Give the extent of all Plasmodium malariae-infected red blood cells.
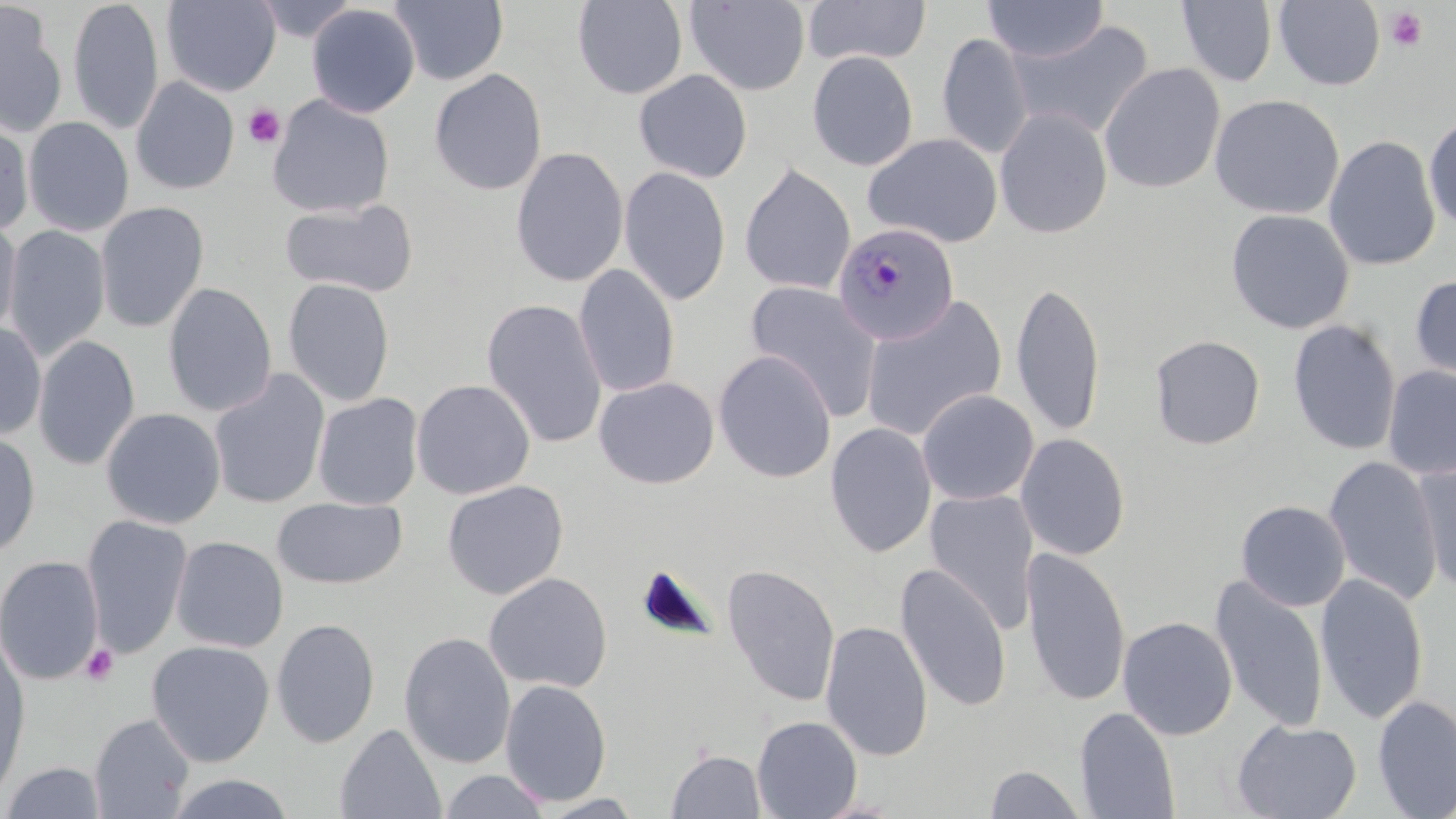
Approximate bounding boxes as named x1/y1/x2/y2 corners in pixels.
Plasmodium malariae-infected red blood cells: (x1=832, y1=222, x2=959, y2=345).

Uninfected red blood cell locations: (x1=68, y1=0, x2=165, y2=136), (x1=161, y1=0, x2=282, y2=97), (x1=251, y1=0, x2=362, y2=41), (x1=388, y1=0, x2=509, y2=86), (x1=802, y1=0, x2=930, y2=66), (x1=1274, y1=0, x2=1386, y2=91), (x1=573, y1=1, x2=688, y2=99), (x1=685, y1=1, x2=810, y2=96), (x1=983, y1=1, x2=1108, y2=63), (x1=1176, y1=1, x2=1278, y2=87), (x1=0, y1=2, x2=68, y2=137), (x1=306, y1=3, x2=420, y2=118), (x1=1005, y1=18, x2=1155, y2=140), (x1=936, y1=33, x2=1034, y2=159), (x1=807, y1=51, x2=919, y2=171), (x1=1099, y1=63, x2=1225, y2=194), (x1=429, y1=69, x2=547, y2=195), (x1=634, y1=69, x2=753, y2=183), (x1=131, y1=76, x2=239, y2=195), (x1=267, y1=94, x2=394, y2=218), (x1=1209, y1=94, x2=1345, y2=220), (x1=994, y1=107, x2=1113, y2=239), (x1=1423, y1=114, x2=1456, y2=232), (x1=0, y1=115, x2=34, y2=236), (x1=23, y1=116, x2=134, y2=237), (x1=864, y1=133, x2=1003, y2=248), (x1=1323, y1=135, x2=1441, y2=271), (x1=510, y1=146, x2=628, y2=287), (x1=739, y1=164, x2=855, y2=295), (x1=619, y1=166, x2=731, y2=306), (x1=279, y1=198, x2=419, y2=298), (x1=94, y1=201, x2=209, y2=333), (x1=1225, y1=209, x2=1355, y2=334), (x1=0, y1=218, x2=22, y2=341), (x1=3, y1=225, x2=111, y2=362), (x1=574, y1=264, x2=680, y2=399), (x1=1410, y1=274, x2=1456, y2=387), (x1=282, y1=277, x2=395, y2=407), (x1=1011, y1=280, x2=1106, y2=439), (x1=744, y1=281, x2=882, y2=422), (x1=162, y1=283, x2=278, y2=417), (x1=861, y1=296, x2=1007, y2=443), (x1=482, y1=298, x2=608, y2=450), (x1=1287, y1=319, x2=1401, y2=456), (x1=0, y1=321, x2=46, y2=440), (x1=33, y1=335, x2=141, y2=471), (x1=1149, y1=335, x2=1266, y2=449), (x1=713, y1=350, x2=837, y2=483), (x1=1382, y1=366, x2=1456, y2=480), (x1=208, y1=370, x2=330, y2=511), (x1=594, y1=377, x2=719, y2=489), (x1=411, y1=379, x2=535, y2=500), (x1=917, y1=389, x2=1039, y2=505), (x1=312, y1=392, x2=424, y2=510), (x1=101, y1=407, x2=225, y2=529), (x1=825, y1=422, x2=937, y2=558), (x1=0, y1=430, x2=41, y2=562), (x1=1015, y1=432, x2=1131, y2=560), (x1=1322, y1=455, x2=1444, y2=606), (x1=1411, y1=460, x2=1455, y2=597), (x1=441, y1=479, x2=569, y2=599), (x1=924, y1=488, x2=1040, y2=634), (x1=271, y1=496, x2=408, y2=589), (x1=1235, y1=499, x2=1351, y2=612), (x1=81, y1=514, x2=193, y2=658), (x1=170, y1=535, x2=289, y2=653), (x1=1020, y1=546, x2=1131, y2=707), (x1=0, y1=555, x2=104, y2=686), (x1=721, y1=563, x2=841, y2=707), (x1=895, y1=563, x2=1012, y2=712), (x1=483, y1=572, x2=612, y2=693), (x1=1315, y1=573, x2=1429, y2=725), (x1=1210, y1=575, x2=1329, y2=732), (x1=1117, y1=616, x2=1238, y2=740), (x1=271, y1=618, x2=380, y2=748), (x1=820, y1=620, x2=934, y2=761), (x1=399, y1=631, x2=517, y2=768), (x1=0, y1=636, x2=31, y2=805), (x1=146, y1=640, x2=275, y2=767), (x1=499, y1=679, x2=612, y2=806), (x1=1373, y1=695, x2=1456, y2=818), (x1=1075, y1=706, x2=1180, y2=819), (x1=89, y1=713, x2=195, y2=819), (x1=751, y1=716, x2=862, y2=819), (x1=1231, y1=718, x2=1362, y2=818), (x1=334, y1=723, x2=447, y2=818), (x1=666, y1=749, x2=766, y2=818), (x1=2, y1=761, x2=107, y2=819), (x1=984, y1=765, x2=1086, y2=818), (x1=438, y1=769, x2=552, y2=818), (x1=164, y1=773, x2=296, y2=818), (x1=534, y1=793, x2=647, y2=818). Platelet locations: (x1=1385, y1=7, x2=1427, y2=53), (x1=243, y1=104, x2=286, y2=149), (x1=80, y1=644, x2=119, y2=685). Slide-level diagnosis: Plasmodium malariae. May-Grünwald-Giemsa stain. Image is 1456×819 pixels. Captured at 1000x magnification. Thin blood smear. Optical microscopy. Single field of view.